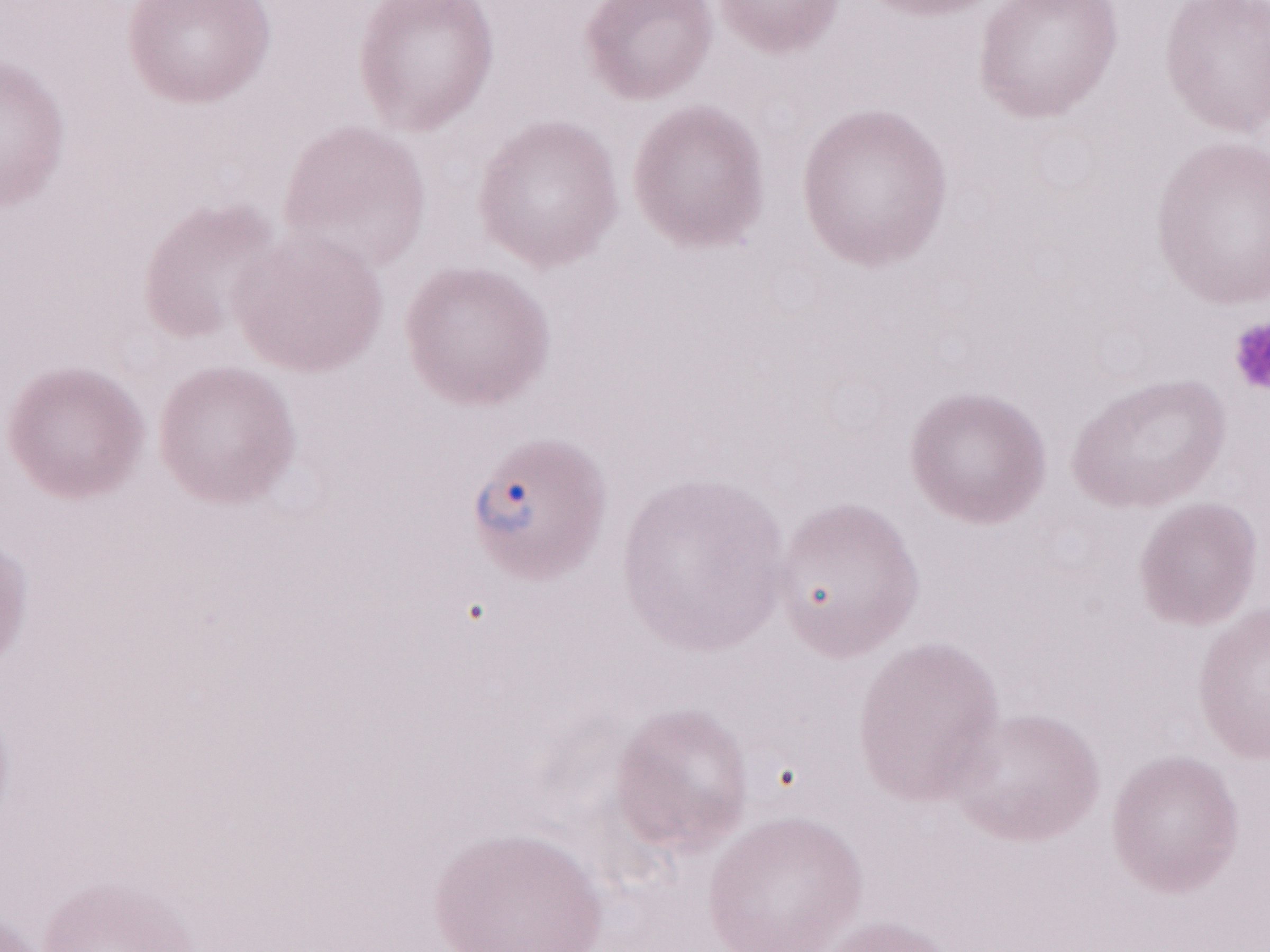

Thin peripheral-blood smear. May-Grünwald-Giemsa (MGG) stain. Malaria diagnosis (patient-level): positive. One field of this slide. Image is 1270×952 pixels. Olympus BX43 microscope and DP73 digital camera. 1,000x magnification.